Assess the morphology of the red blood cells.
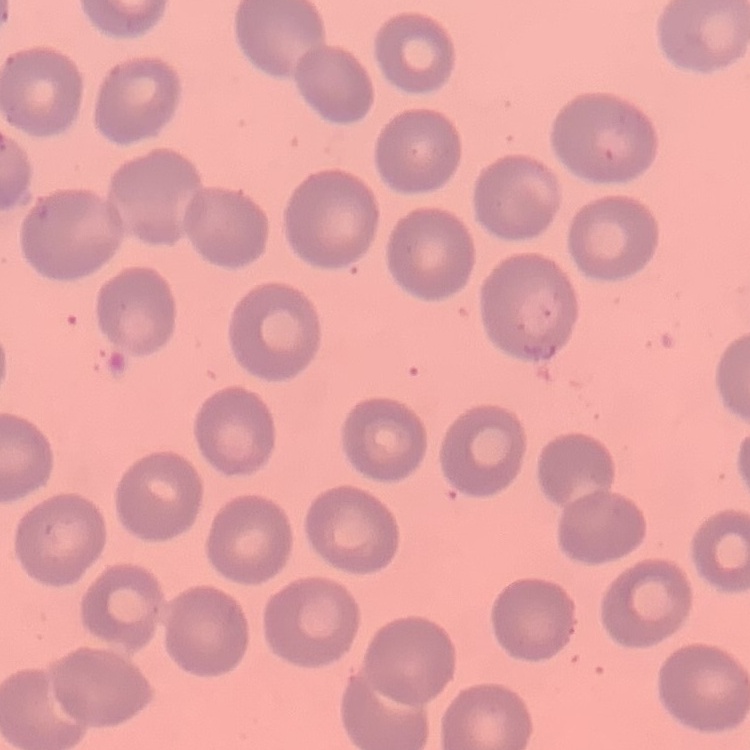
They show no rouleaux formation.

{
  "preparation": "thin blood film",
  "stain": "Field's or Giemsa",
  "image_type": "square crop of a larger photomicrograph"
}